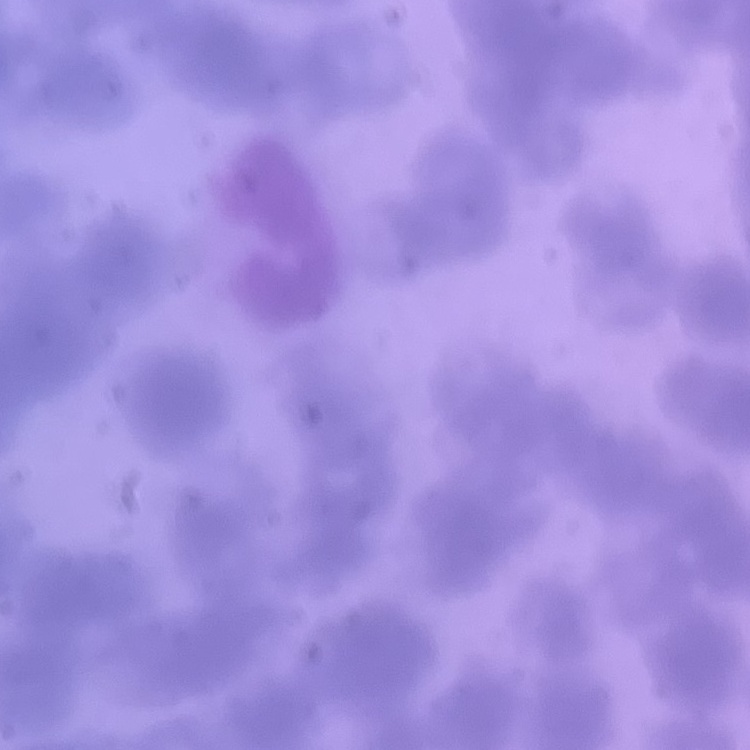

erythrocyte morphology = rouleaux formation
stain = Field's or Giemsa
preparation = thin blood smear
image type = square crop of a larger photomicrograph